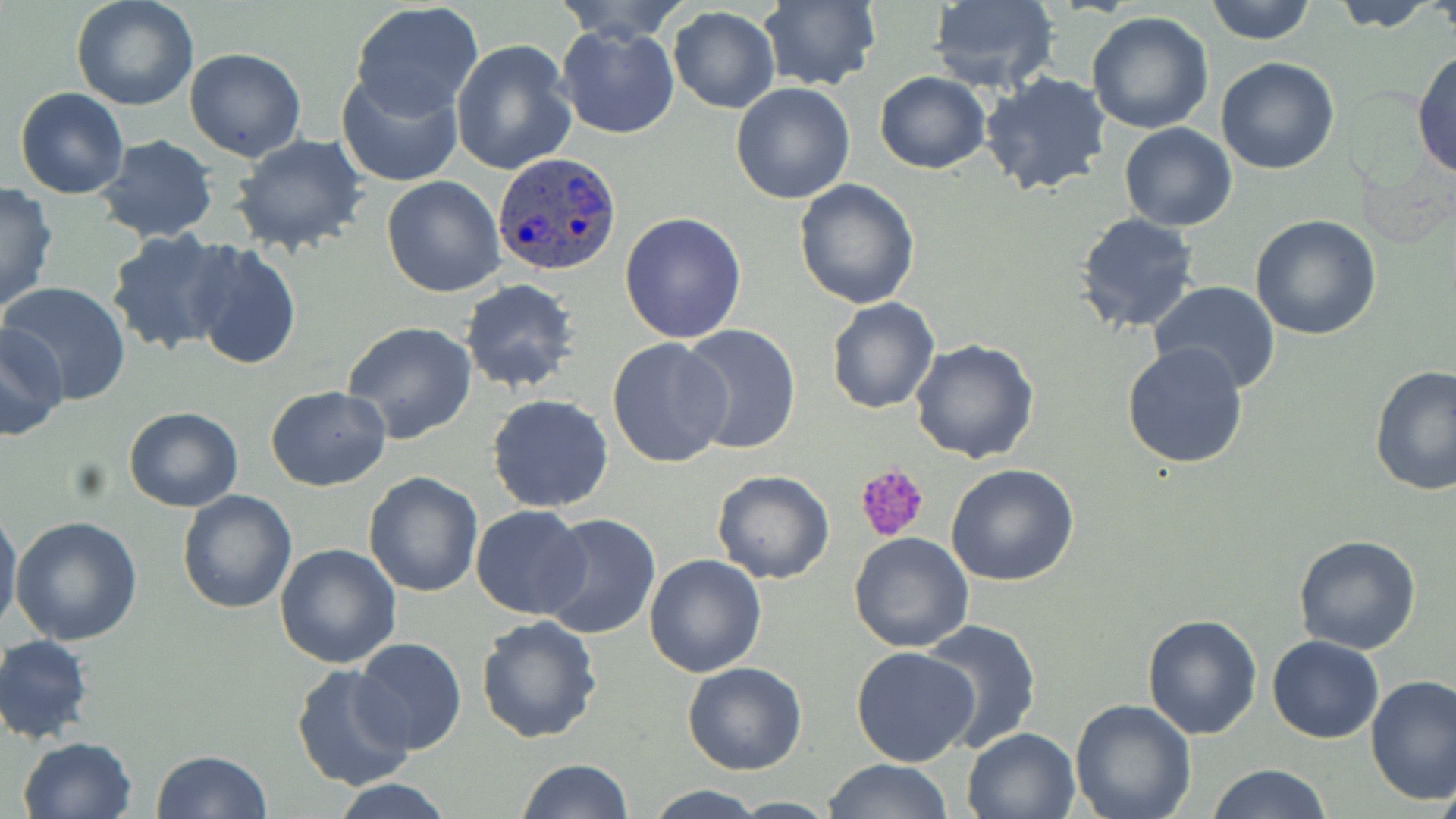
Approximate bounding boxes as (x1,y1)-(x2,y2) corner pairs in pixels. Platelet locations: (855,462)-(931,544). Uninfected red blood cell locations: (70,0)-(200,111), (554,0)-(691,43), (926,0)-(1061,94), (1203,0)-(1316,45), (1324,0)-(1440,30), (351,1)-(484,119), (756,1)-(880,89), (667,7)-(780,113), (1086,9)-(1216,134), (556,23)-(680,140), (451,39)-(577,177), (1412,46)-(1456,182), (185,47)-(308,162), (1215,57)-(1340,175), (335,70)-(464,188), (979,71)-(1112,197), (874,72)-(992,174), (731,83)-(857,203), (15,87)-(129,199), (1119,124)-(1237,231), (231,134)-(369,255), (92,137)-(219,242), (381,176)-(506,297), (793,179)-(920,310), (0,182)-(58,315), (620,211)-(747,342), (1074,211)-(1202,334), (1250,214)-(1383,340), (105,230)-(238,355), (188,243)-(301,370), (460,278)-(581,394), (1149,281)-(1280,392), (3,282)-(132,405), (826,298)-(939,415), (343,320)-(477,443), (678,323)-(801,454), (0,325)-(69,441), (606,337)-(732,469), (910,339)-(1040,464), (1120,340)-(1250,469), (1370,365)-(1456,499), (266,385)-(392,492), (487,394)-(616,513), (123,407)-(244,511), (946,464)-(1079,586), (712,470)-(835,584), (363,471)-(483,597), (177,491)-(297,614), (470,506)-(591,619), (1,508)-(23,636), (539,512)-(661,640), (11,517)-(143,647), (848,531)-(972,651), (1293,535)-(1422,655), (274,543)-(402,667), (644,554)-(768,677), (1141,612)-(1263,739), (475,614)-(602,741), (916,619)-(1043,753), (1,634)-(96,745), (1267,634)-(1383,743), (354,638)-(466,755), (851,647)-(981,766), (682,660)-(807,776), (290,664)-(416,792), (1366,676)-(1456,807), (1069,700)-(1197,819), (960,727)-(1081,819), (18,735)-(139,819), (153,749)-(272,819), (517,758)-(635,819), (823,759)-(953,818), (1432,761)-(1456,819), (1204,763)-(1331,819), (328,777)-(457,818), (643,784)-(768,819), (726,796)-(839,816). Plasmodium ovale-infected red blood cell locations: (492,152)-(621,279). Slide-level diagnosis: Plasmodium ovale. May-Grünwald-Giemsa-stained preparation. One field of a larger specimen. 1000x magnification. Image is 1456×819 pixels. Thin blood smear. Optical microscopy.